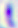

Toxoplasma gondii is shown. Photomicrograph. 400x magnification.